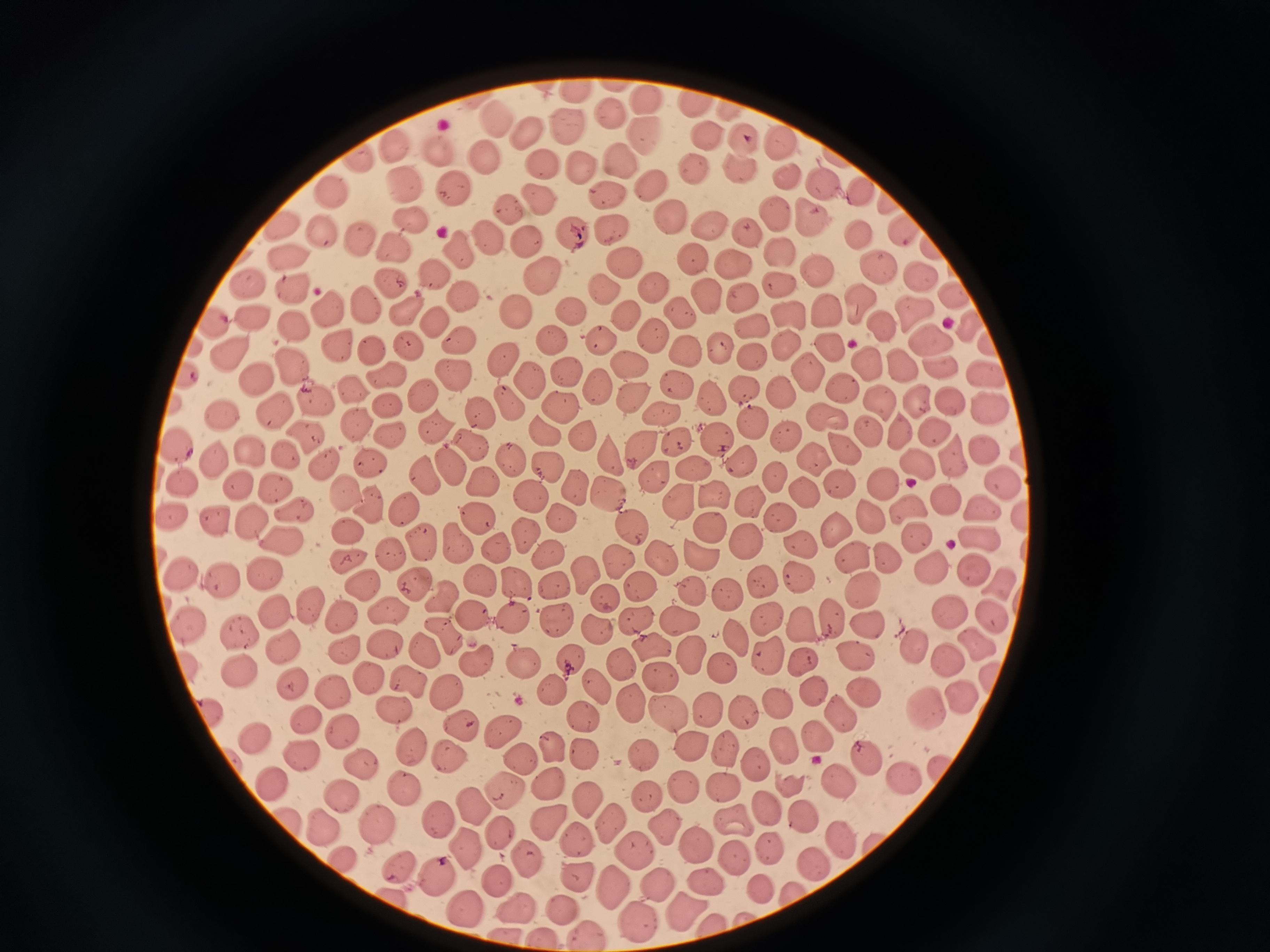

Approximate object centers, in pixels from the top-left corner.
Summary:
  - Cell locations: (x=615, y=83), (x=575, y=91), (x=643, y=99), (x=696, y=103), (x=730, y=111), (x=608, y=112), (x=495, y=121), (x=567, y=125), (x=524, y=132), (x=645, y=135), (x=705, y=135), (x=784, y=145), (x=741, y=146), (x=394, y=149), (x=436, y=150), (x=481, y=160), (x=542, y=160), (x=361, y=161), (x=580, y=164), (x=618, y=164), (x=735, y=166), (x=692, y=170), (x=787, y=177), (x=823, y=183), (x=651, y=187), (x=333, y=189), (x=403, y=189), (x=607, y=190), (x=449, y=192), (x=859, y=192), (x=538, y=203), (x=887, y=203), (x=510, y=211), (x=772, y=214), (x=811, y=216), (x=668, y=219), (x=706, y=225), (x=280, y=226), (x=412, y=226), (x=611, y=229), (x=899, y=229), (x=571, y=232), (x=747, y=235), (x=322, y=237), (x=488, y=237), (x=858, y=238), (x=361, y=242), (x=525, y=242), (x=394, y=244), (x=931, y=247), (x=458, y=249), (x=777, y=252), (x=287, y=257), (x=691, y=263), (x=619, y=264), (x=735, y=265), (x=879, y=268), (x=817, y=270), (x=540, y=275), (x=917, y=275), (x=439, y=276), (x=390, y=283), (x=246, y=284), (x=776, y=284), (x=601, y=287), (x=648, y=288), (x=289, y=290), (x=706, y=295), (x=953, y=295), (x=742, y=296), (x=466, y=301), (x=855, y=301), (x=366, y=304), (x=402, y=310), (x=911, y=310), (x=330, y=311), (x=518, y=312), (x=569, y=312), (x=825, y=312), (x=251, y=314), (x=625, y=317), (x=786, y=317), (x=680, y=319), (x=292, y=323), (x=884, y=323), (x=214, y=324), (x=432, y=324), (x=749, y=325), (x=655, y=334), (x=928, y=336), (x=552, y=338), (x=784, y=339), (x=456, y=342), (x=599, y=342), (x=335, y=345), (x=406, y=345), (x=828, y=346), (x=370, y=349), (x=686, y=350), (x=720, y=351), (x=226, y=356), (x=754, y=358), (x=501, y=359), (x=628, y=364), (x=868, y=364), (x=288, y=365), (x=903, y=368), (x=939, y=369), (x=382, y=374), (x=451, y=374), (x=565, y=374), (x=808, y=375), (x=527, y=377), (x=189, y=378), (x=984, y=378), (x=253, y=382), (x=674, y=385), (x=599, y=386), (x=353, y=387), (x=842, y=389), (x=744, y=391), (x=783, y=392), (x=422, y=394), (x=708, y=396), (x=313, y=398), (x=919, y=398), (x=630, y=401), (x=876, y=402), (x=953, y=402), (x=508, y=405), (x=386, y=406), (x=560, y=408), (x=985, y=408), (x=663, y=411), (x=477, y=413), (x=217, y=416), (x=274, y=418), (x=355, y=421), (x=825, y=421), (x=753, y=426), (x=428, y=427), (x=544, y=431), (x=871, y=433), (x=903, y=433), (x=936, y=433), (x=391, y=435), (x=303, y=436), (x=583, y=438), (x=719, y=439), (x=783, y=439), (x=640, y=440), (x=677, y=441), (x=465, y=443), (x=837, y=445), (x=176, y=448), (x=248, y=450), (x=986, y=450), (x=282, y=452), (x=611, y=455), (x=507, y=457), (x=813, y=459), (x=916, y=459), (x=216, y=460), (x=954, y=460), (x=368, y=462), (x=319, y=463), (x=740, y=463), (x=452, y=466), (x=546, y=467), (x=695, y=469), (x=655, y=474), (x=420, y=477), (x=237, y=481), (x=1000, y=481), (x=884, y=482), (x=770, y=483), (x=181, y=484), (x=277, y=486), (x=572, y=486), (x=836, y=486), (x=483, y=488), (x=344, y=492), (x=611, y=492), (x=531, y=495), (x=712, y=496), (x=804, y=498), (x=946, y=498), (x=750, y=502), (x=678, y=503), (x=372, y=506), (x=406, y=507), (x=906, y=507), (x=982, y=507), (x=173, y=512), (x=292, y=512), (x=781, y=517), (x=559, y=518), (x=1023, y=518), (x=872, y=520), (x=218, y=521), (x=475, y=521), (x=254, y=522), (x=708, y=528), (x=629, y=530), (x=832, y=530), (x=344, y=532), (x=979, y=534), (x=525, y=536), (x=417, y=538), (x=914, y=540), (x=747, y=541), (x=454, y=542), (x=285, y=545), (x=498, y=546), (x=797, y=546), (x=545, y=549), (x=390, y=554), (x=696, y=556), (x=664, y=558), (x=851, y=559), (x=885, y=559), (x=347, y=563), (x=621, y=564), (x=929, y=566), (x=976, y=566), (x=181, y=570), (x=583, y=571), (x=798, y=575), (x=262, y=576), (x=480, y=578), (x=220, y=580), (x=516, y=581), (x=764, y=581), (x=364, y=584), (x=1003, y=584), (x=416, y=585), (x=555, y=585), (x=639, y=586), (x=691, y=589), (x=863, y=593), (x=727, y=594), (x=607, y=596), (x=447, y=601), (x=310, y=607), (x=388, y=611), (x=474, y=612), (x=512, y=612), (x=277, y=614), (x=344, y=614), (x=992, y=614), (x=830, y=616), (x=680, y=617), (x=555, y=618), (x=635, y=620), (x=190, y=622), (x=765, y=622), (x=803, y=623), (x=597, y=628), (x=867, y=629), (x=244, y=632), (x=738, y=636), (x=443, y=639), (x=976, y=641), (x=281, y=647), (x=649, y=647), (x=424, y=648), (x=390, y=649), (x=347, y=650), (x=693, y=653), (x=766, y=656), (x=570, y=657), (x=951, y=658), (x=525, y=660), (x=853, y=660), (x=805, y=661), (x=478, y=662), (x=620, y=664), (x=187, y=666), (x=723, y=666), (x=240, y=668), (x=657, y=673), (x=371, y=677), (x=407, y=678), (x=289, y=680), (x=597, y=687), (x=811, y=688), (x=333, y=691), (x=447, y=691), (x=552, y=691), (x=961, y=691), (x=861, y=694), (x=630, y=701), (x=773, y=701), (x=392, y=706), (x=707, y=706), (x=669, y=711), (x=206, y=712), (x=743, y=712), (x=927, y=712), (x=839, y=714), (x=581, y=717), (x=313, y=722), (x=460, y=727), (x=501, y=732), (x=818, y=735), (x=344, y=736), (x=259, y=739), (x=783, y=741), (x=549, y=744), (x=411, y=747), (x=581, y=748), (x=726, y=748), (x=691, y=749), (x=302, y=752), (x=452, y=754), (x=642, y=755), (x=518, y=758), (x=869, y=759), (x=756, y=760), (x=360, y=764), (x=940, y=768), (x=905, y=779), (x=845, y=780), (x=275, y=781), (x=786, y=782), (x=548, y=784), (x=402, y=787), (x=725, y=787), (x=501, y=789), (x=684, y=789), (x=343, y=792), (x=646, y=796), (x=586, y=798), (x=470, y=802), (x=763, y=807), (x=442, y=814), (x=734, y=820), (x=807, y=821), (x=548, y=822), (x=607, y=822), (x=380, y=823), (x=324, y=824), (x=661, y=825), (x=499, y=833), (x=837, y=837), (x=578, y=838), (x=693, y=843), (x=770, y=846), (x=464, y=847), (x=634, y=854), (x=734, y=855), (x=346, y=858), (x=527, y=859), (x=814, y=862), (x=396, y=863), (x=435, y=872), (x=579, y=877), (x=496, y=880), (x=700, y=883), (x=608, y=885), (x=655, y=885), (x=760, y=888), (x=794, y=893), (x=393, y=894), (x=565, y=906), (x=517, y=907), (x=466, y=908), (x=678, y=912), (x=636, y=924), (x=717, y=924), (x=583, y=933), (x=542, y=935)
  - Image size: 1270×952 pixels
  - Preparation: thin blood film
  - Stain: Giemsa
  - Capture: smartphone through the microscope eyepiece
  - Field of view: single